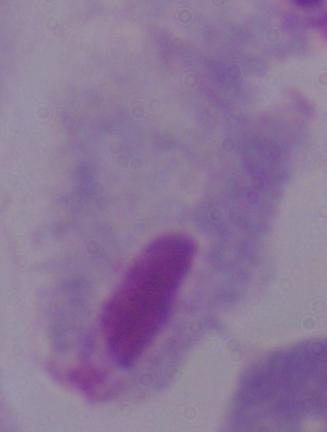
{
  "modality": "photomicrograph",
  "magnification": "1000x",
  "identification": "trichomonad"
}